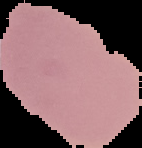
Malaria status: uninfected. Image is 142×148 pixels. The area outside the segmented cell region is set to black. From a thin blood film.